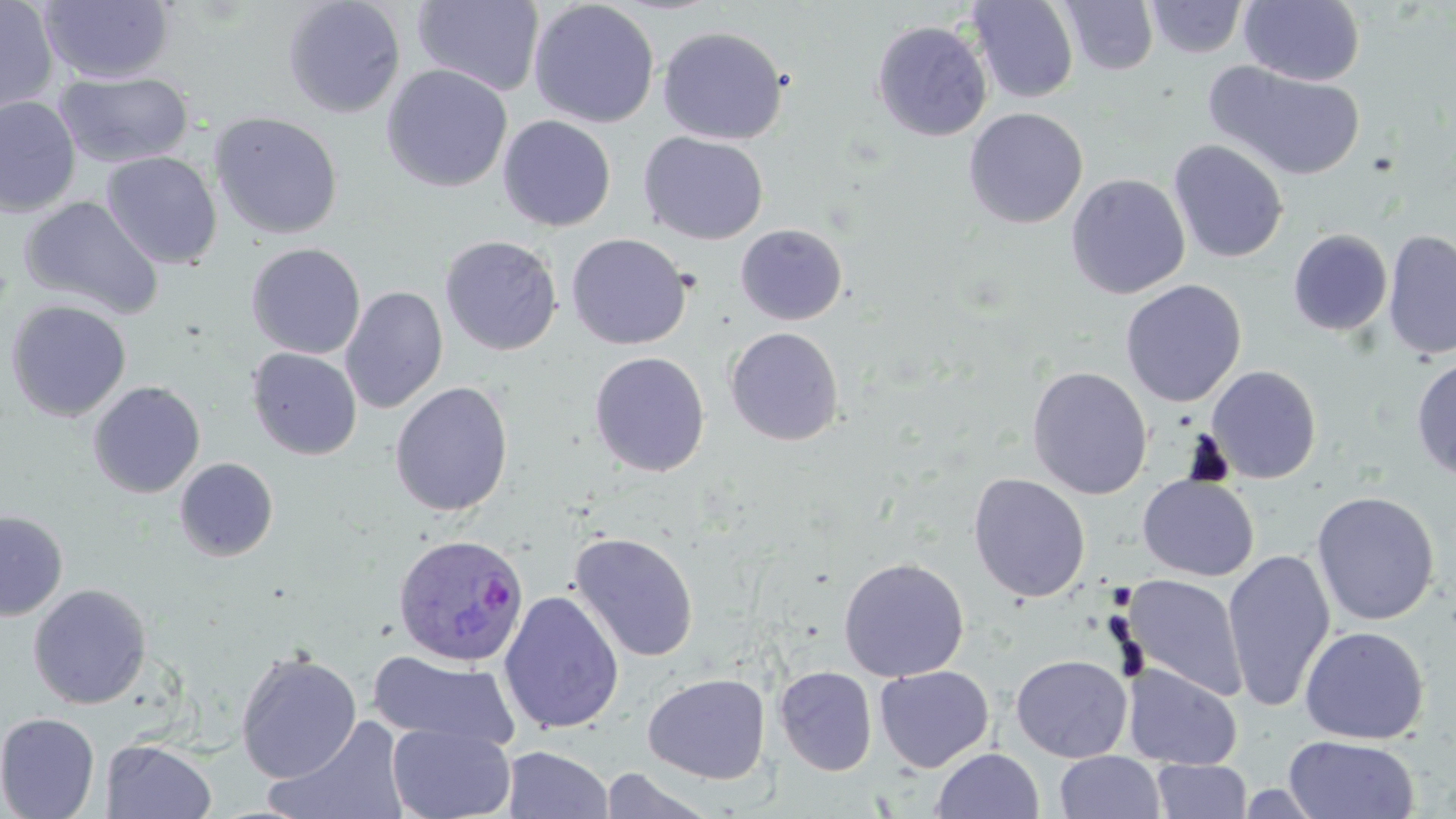
Summary:
  - Coordinate format: approximate bounding boxes as (x1,y1)-(x2,y2) corner pairs in pixels
  - Plasmodium ovale-infected red blood cell locations: (392,533)-(530,667)
  - Uninfected red blood cell locations: (0,0)-(59,116), (38,0)-(175,84), (282,0)-(406,118), (412,0)-(545,96), (967,0)-(1079,104), (528,1)-(659,128), (1059,1)-(1159,75), (1146,1)-(1247,58), (1239,1)-(1366,86), (871,20)-(992,141), (657,26)-(788,145), (1204,61)-(1366,181), (381,64)-(512,193), (54,70)-(194,169), (0,97)-(81,217), (963,107)-(1088,229), (208,112)-(343,240), (498,115)-(616,232), (639,132)-(769,244), (1168,139)-(1289,264), (101,151)-(222,269), (1066,173)-(1190,299), (20,196)-(164,321), (735,224)-(848,325), (1287,228)-(1393,336), (1383,230)-(1456,361), (566,233)-(691,350), (440,235)-(562,356), (245,242)-(366,359), (1120,279)-(1247,407), (340,286)-(448,414), (5,299)-(132,422), (725,326)-(845,446), (246,347)-(363,460), (589,351)-(710,476), (1411,355)-(1456,483), (1207,365)-(1321,483), (1027,366)-(1153,499), (87,380)-(206,498), (390,381)-(513,517), (174,457)-(279,562), (968,473)-(1091,602), (1138,475)-(1259,581), (1312,491)-(1440,626), (0,510)-(68,621), (569,532)-(699,663), (1222,549)-(1336,713), (838,557)-(969,681), (1124,575)-(1248,702), (28,583)-(152,709), (499,590)-(624,734), (1299,625)-(1430,744), (235,649)-(362,782), (367,650)-(520,750), (1011,654)-(1132,762), (1122,663)-(1242,769), (774,666)-(877,776), (875,666)-(993,772), (643,672)-(770,784), (0,712)-(101,819), (270,717)-(408,818), (387,723)-(516,819), (1283,735)-(1419,818), (102,739)-(217,819), (502,745)-(613,818), (930,747)-(1044,819), (1054,751)-(1166,819), (1151,760)-(1253,818), (598,769)-(721,818)
  - Slide-level diagnosis: Plasmodium ovale
  - Preparation: thin blood film
  - Magnification: 1000x
  - Modality: optical microscopy
  - Image size: 1456×819 pixels
  - Stain: May-Grünwald-Giemsa
  - Field of view: one of a larger specimen